Report the malaria status of this cell.
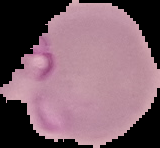
Parasitized.

preparation = thin blood smear
image type = segmented cell region with the area outside set to black
image size = 160×148 pixels